Outline each blood parasite and name the species.
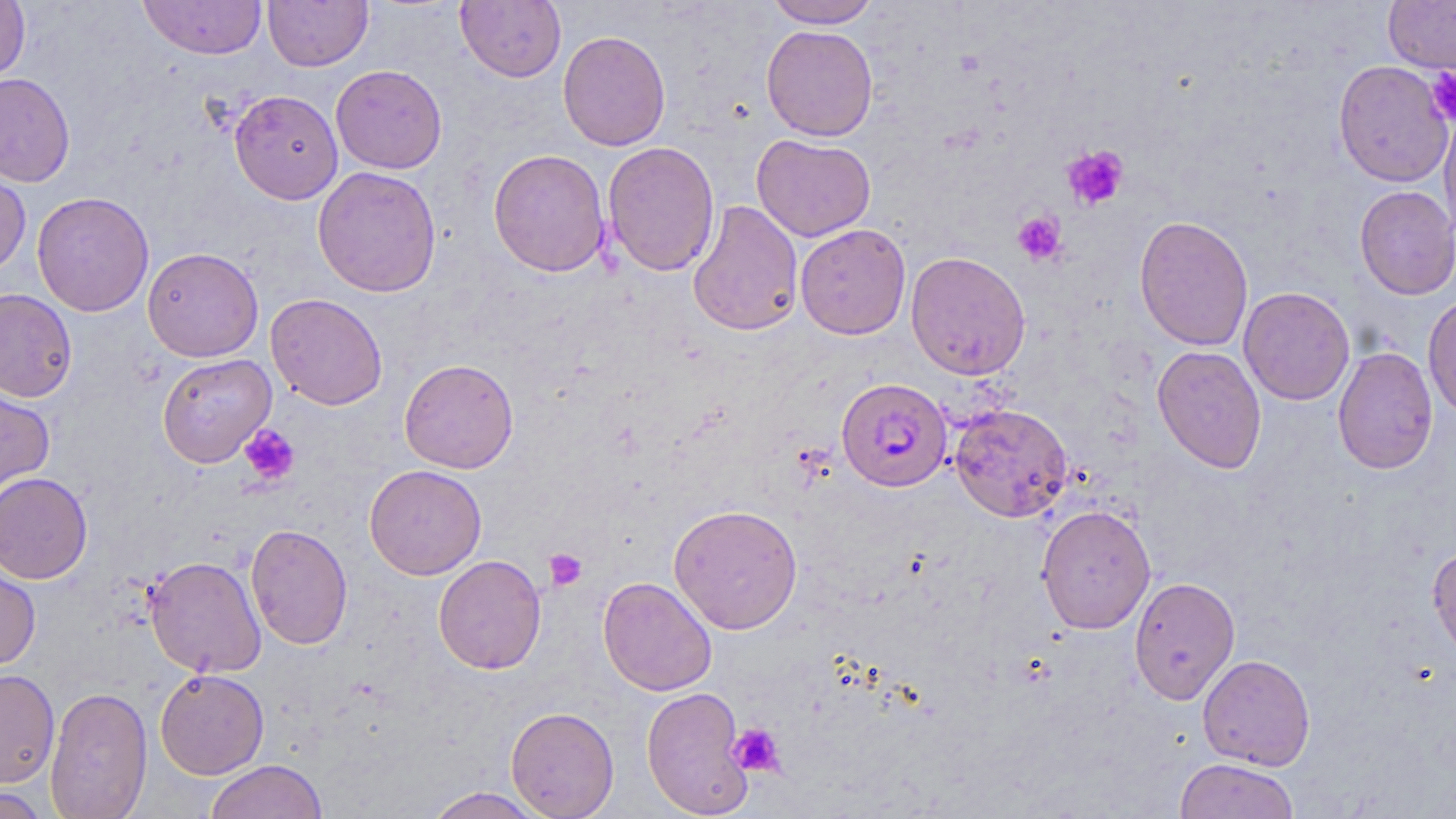
Approximate bounding boxes as [x1, y1, x2, y2] in pixels.
Plasmodium falciparum-infected red blood cells: [837, 378, 953, 492].
No Plasmodium ovale, Plasmodium malariae, Plasmodium vivax, Babesia divergens, or Trypanosoma brucei observed.

Platelet locations: [1426, 67, 1456, 125], [1062, 145, 1129, 210], [1012, 211, 1067, 265], [239, 423, 301, 487], [544, 548, 588, 591], [728, 722, 785, 777]. Uninfected red blood cell locations: [0, 0, 30, 83], [138, 0, 267, 60], [263, 0, 373, 71], [765, 0, 881, 28], [1383, 0, 1456, 75], [455, 1, 566, 83], [761, 24, 879, 141], [557, 30, 671, 151], [1333, 59, 1454, 187], [331, 64, 447, 174], [0, 73, 75, 187], [229, 89, 343, 204], [1439, 108, 1456, 240], [751, 133, 877, 242], [603, 141, 720, 277], [488, 148, 611, 277], [0, 162, 31, 278], [313, 166, 441, 297], [1354, 185, 1456, 300], [32, 191, 154, 317], [687, 199, 804, 337], [1134, 215, 1254, 351], [795, 224, 911, 340], [142, 247, 263, 362], [905, 251, 1031, 380], [1238, 286, 1355, 405], [0, 288, 78, 402], [1422, 292, 1456, 421], [266, 293, 388, 410], [1152, 345, 1267, 474], [1333, 346, 1438, 475], [157, 353, 276, 468], [399, 358, 519, 473], [0, 382, 55, 505], [949, 403, 1073, 522], [364, 464, 486, 579], [0, 472, 93, 584], [668, 503, 803, 634], [1035, 504, 1157, 634], [245, 523, 353, 650], [1427, 544, 1456, 658], [433, 554, 546, 675], [145, 555, 266, 678], [0, 559, 41, 672], [598, 576, 717, 696], [1129, 576, 1240, 704], [1197, 654, 1316, 771], [0, 668, 60, 787], [155, 669, 269, 779], [45, 686, 152, 818], [641, 686, 753, 817], [505, 706, 619, 818], [1175, 758, 1299, 819], [205, 759, 328, 819], [1, 785, 52, 818], [421, 787, 551, 818]. Slide-level diagnosis: Plasmodium falciparum. 1000x magnification. Thin blood smear. Optical microscopy. One field of a larger specimen. Image is 1456×819 pixels. May-Grünwald-Giemsa-stained preparation.